Assess this cell for malaria.
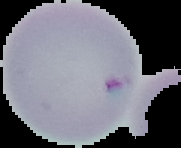
It is uninfected.

Summary:
  - Image type: segmented cell region on a black background
  - Preparation: thin blood smear
  - Image size: 181×148 pixels